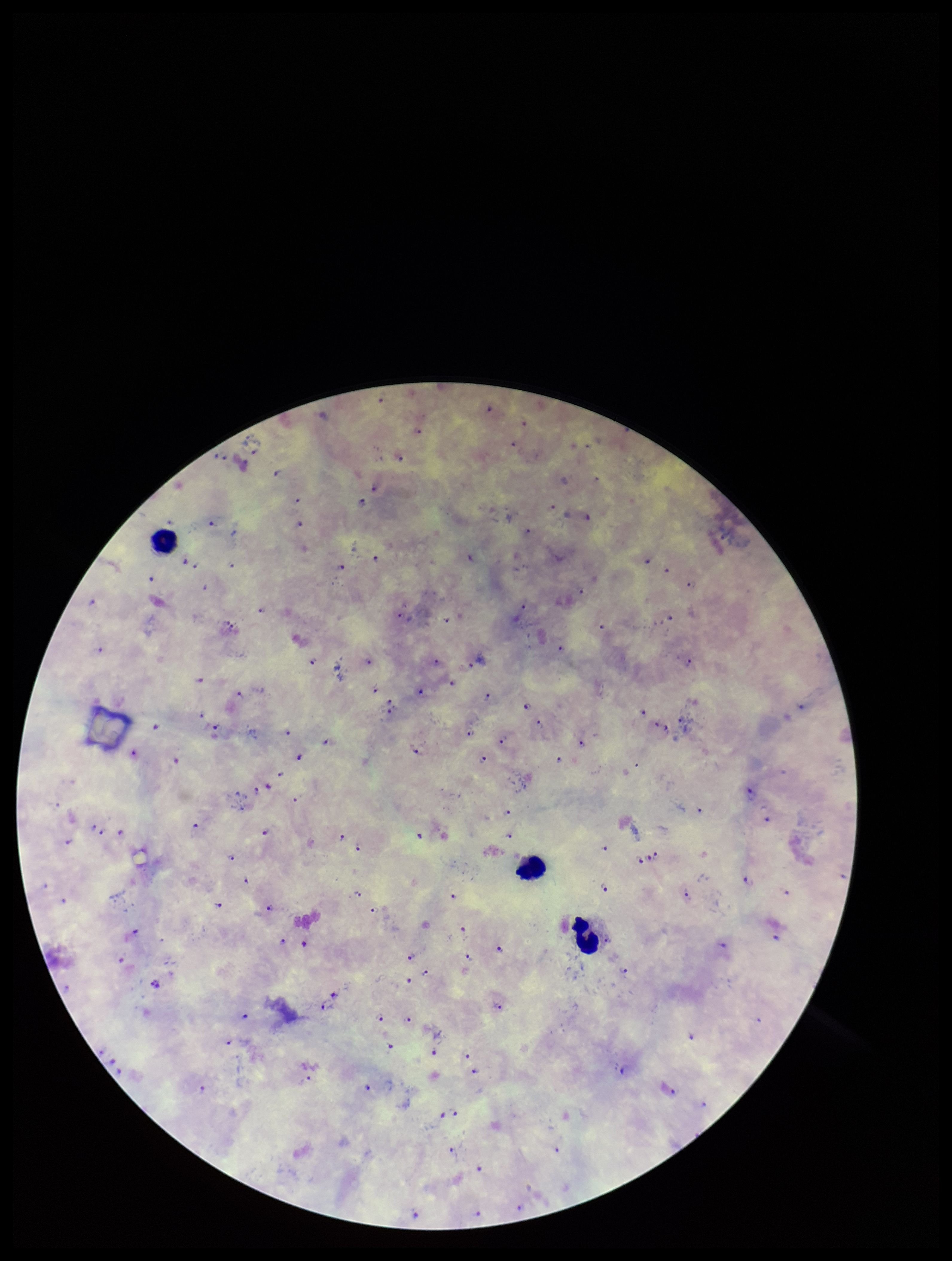
Summary:
  - Stain: Giemsa
  - Plasmodium parasites: detected
  - Parasite count: 119
  - Capture: smartphone photograph through the microscope eyepiece
  - Image size: 952×1261 pixels
  - Preparation: thick blood smear
  - Leukocyte count: 3
  - Patient malaria status: infected
  - Species reported for this patient: Plasmodium falciparum
  - Field of view: one from this slide